Name the parasite shown.
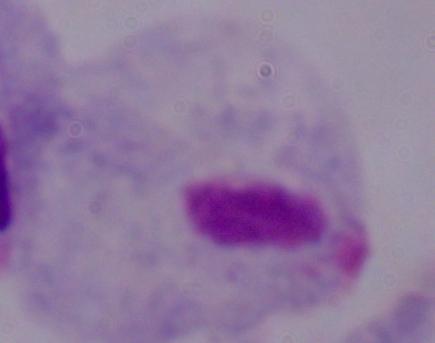
A trichomonad.

1000x magnification. Photomicrograph.